State which parasite is depicted.
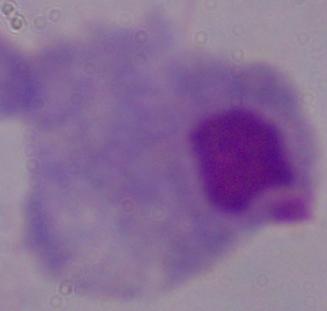
A trichomonad.

modality = micrograph
magnification = 1000x